Classify this cell by malaria status.
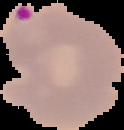
Parasitized.

Image is 124×130 pixels. From a thin blood film. Segmented cell region on a black background.